Find the cells and give the type of each one.
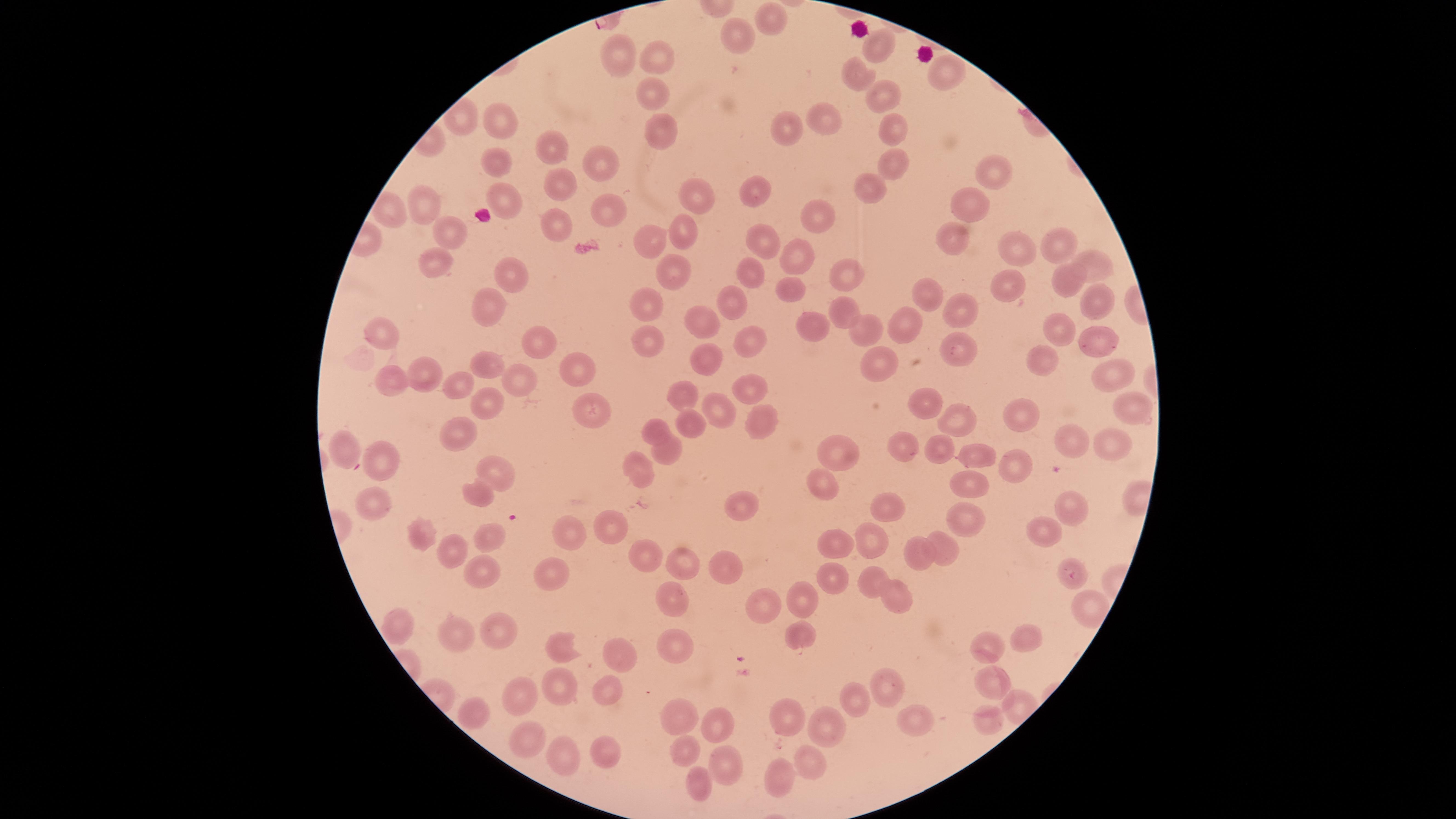

No parasitized red blood cells identified.
Approximate marker points as (x, y) in pixels.
Uninfected red blood cells: (771, 22), (742, 34), (876, 49), (651, 53), (628, 54), (945, 73), (868, 77), (656, 90), (879, 90), (823, 118), (892, 121), (508, 124), (787, 125), (656, 128), (558, 146), (494, 155), (896, 158), (598, 161), (996, 173), (556, 182), (869, 184), (761, 186), (508, 192), (426, 200), (693, 201), (612, 208), (388, 209), (974, 210), (820, 216), (449, 229), (560, 229), (680, 231), (759, 233), (651, 235), (948, 241), (1054, 242), (1016, 245), (795, 250), (1100, 259), (439, 261), (845, 267), (753, 268), (672, 272), (508, 276), (1064, 282), (1002, 285), (789, 289), (1093, 292), (933, 294), (646, 295), (732, 300), (841, 303), (958, 308), (493, 311), (701, 311), (906, 317), (868, 327), (812, 329), (1055, 330), (745, 335), (651, 336), (385, 338), (539, 341), (956, 343), (1094, 345), (708, 354), (868, 359), (1040, 359), (487, 361), (570, 362), (423, 366), (1111, 372), (526, 379), (748, 379), (454, 380), (390, 383), (689, 393), (482, 401), (921, 401), (583, 405), (1131, 408), (720, 410), (1024, 413), (767, 417), (687, 423), (964, 423), (653, 428), (465, 438), (351, 443), (1072, 443), (902, 445), (1114, 445), (936, 447), (668, 453), (839, 454), (389, 458), (980, 458), (636, 464), (1012, 465), (501, 475), (970, 484), (823, 485), (469, 489), (1072, 502), (882, 503), (734, 505), (371, 507), (967, 517), (1047, 523), (613, 526), (493, 532), (423, 533), (569, 535), (871, 541), (837, 545), (942, 545), (454, 552), (921, 553), (685, 559), (639, 560), (725, 565), (483, 570), (554, 573), (1068, 573), (867, 574), (835, 578), (803, 595), (890, 597), (678, 601), (1090, 603), (757, 607), (401, 622), (498, 624), (462, 631), (796, 634), (1020, 640), (563, 643), (988, 645), (677, 646), (616, 656), (878, 681), (995, 683), (611, 686), (558, 687), (519, 692), (856, 702), (677, 708), (470, 713), (783, 716), (909, 718), (988, 722), (716, 728), (828, 728), (523, 735), (685, 749), (555, 751), (613, 752), (806, 760), (725, 764), (773, 774), (700, 782).
No white blood cells identified.

Summary:
  - Field of view: single
  - Image size: 1456×819 pixels
  - Preparation: thin smear of blood
  - Visible region: circular
  - Stain: Giemsa
  - Capture: smartphone photograph through the microscope eyepiece